Assess the morphology of the erythrocytes.
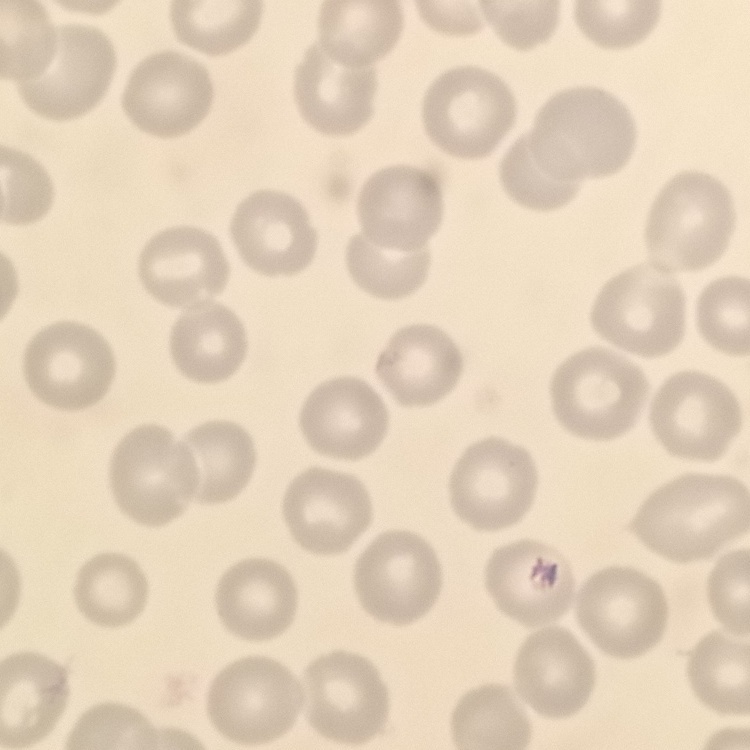
They show no rouleaux formation.

Field's or Giemsa stain. One tile cut from a larger photomicrograph. Thin blood smear.